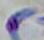
modality = micrograph
identification = Toxoplasma gondii
magnification = 1000x